Name the cell type shown.
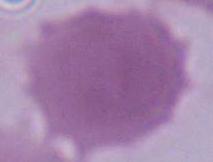
An erythrocyte.

modality = photomicrograph
magnification = 1000x